Name the parasite shown.
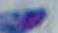
This is Toxoplasma gondii.

magnification = 1000x
modality = photomicrograph